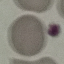

result = negative for malaria parasites
preparation = thin blood smear
stain = Giemsa
capture = smartphone camera at the microscope eyepiece
image type = automatically extracted cell patch, resized to 64 × 64 pixels